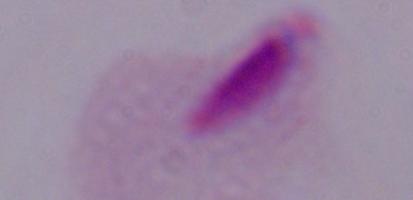
Summary:
  - Modality: photomicrograph
  - Magnification: 1000x
  - Identification: trichomonad